Report the malaria status of this cell.
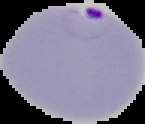

It is parasitized.

Summary:
  - Image size: 145×124 pixels
  - Preparation: thin blood smear
  - Image type: cell region segmented out of the field of view; surrounding area masked to black